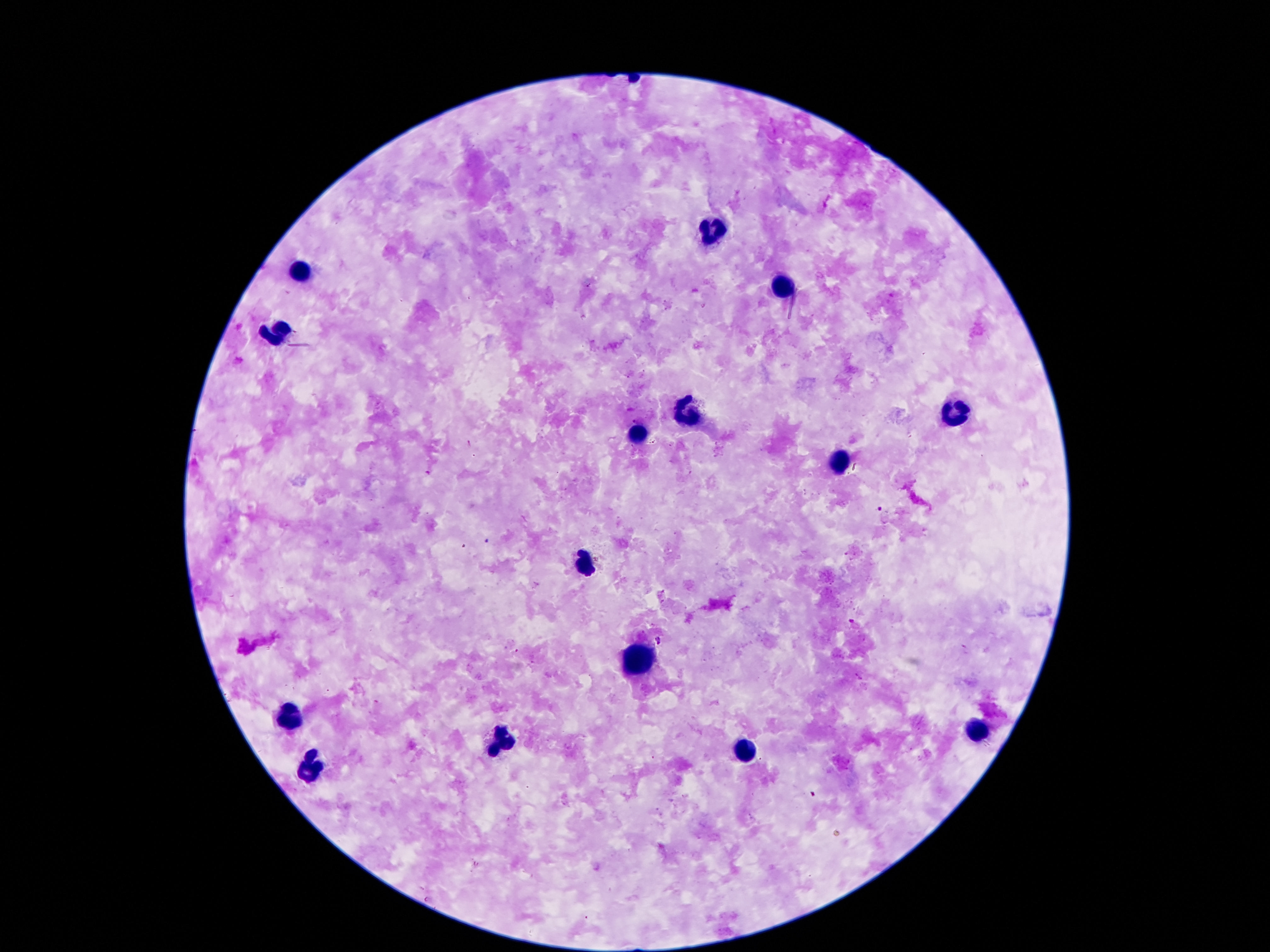
magnification = 100x
preparation = thick blood film
capture = smartphone camera through the microscope eyepiece
stain = Giemsa
field of view = single
leukocyte locations = approximate object centers, in pixels from the top-left corner: (x=712, y=232), (x=302, y=271), (x=779, y=286), (x=281, y=329), (x=953, y=411), (x=688, y=413), (x=639, y=431), (x=837, y=465), (x=585, y=560), (x=636, y=657), (x=289, y=719), (x=977, y=728), (x=503, y=741), (x=742, y=750), (x=315, y=768)
patient malaria status = negative
image size = 1270×952 pixels